Locate every Plasmodium parasite.
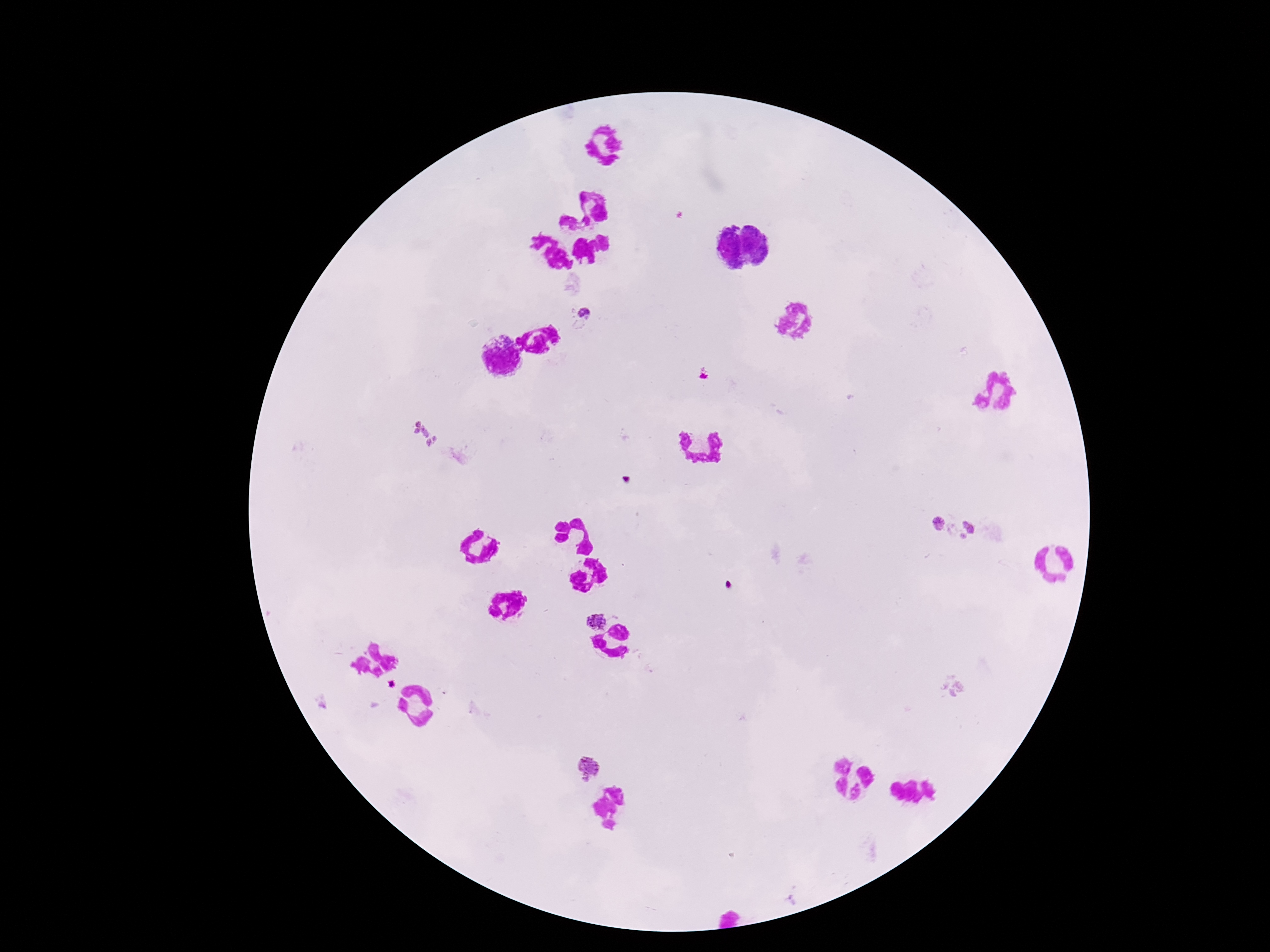
Approximate centers as (x, y) in pixels.
Plasmodium parasites: (583, 316), (702, 375), (425, 434), (939, 523), (976, 530), (954, 687), (589, 768).

Summary:
  - Image size: 1270×952 pixels
  - Preparation: thick peripheral-blood smear
  - Magnification: 100x
  - Field of view: single
  - Capture: smartphone camera through the microscope eyepiece
  - Stain: Giemsa
  - Patient malaria status: positive